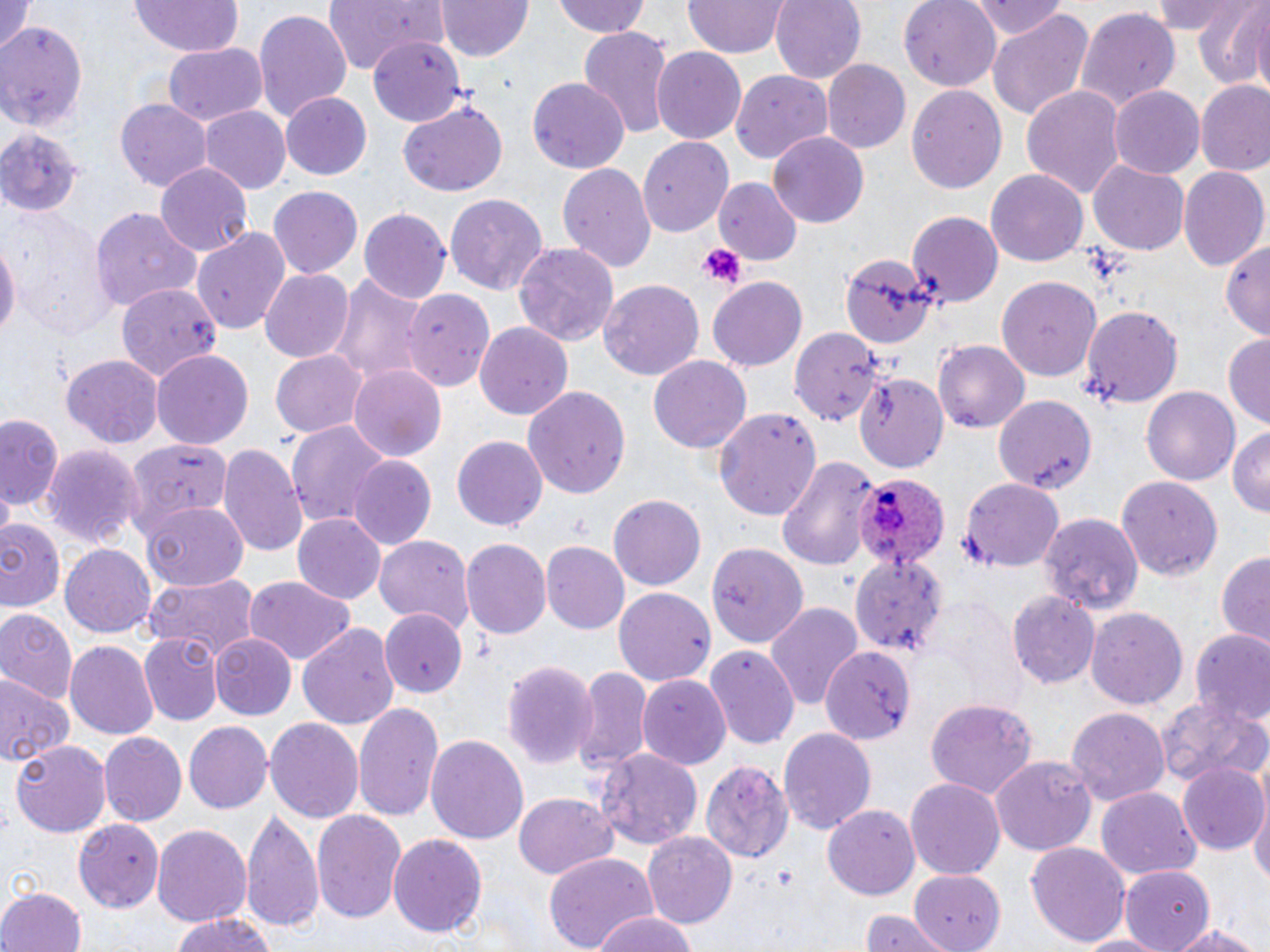
plasmodium_ovale_infected_red_blood_cell_locations: 'approximate bounding boxes as (x1, y1, x2, y2) in pixels: (854, 470, 955, 577)'
slide_level_diagnosis: Plasmodium ovale
modality: light microscopy
field_of_view: one of a larger specimen
platelet_locations: 'approximate bounding boxes as (x1, y1, x2, y2) in pixels: (699, 242, 745, 289)'
uninfected_red_blood_cell_locations: 'approximate bounding boxes as (x1, y1, x2, y2) in pixels: (325, 0, 448, 74), (438, 0, 533, 62), (552, 0, 653, 39), (771, 0, 866, 83), (900, 0, 1003, 89), (975, 0, 1066, 41), (1150, 0, 1252, 36), (1190, 0, 1270, 90), (0, 1, 33, 60), (129, 1, 242, 58), (683, 1, 788, 58), (145, 2, 256, 109), (1244, 6, 1270, 100), (1072, 7, 1182, 114), (253, 8, 353, 122), (987, 8, 1095, 122), (0, 19, 85, 134), (576, 28, 673, 138), (370, 38, 463, 125), (161, 43, 267, 126), (651, 46, 747, 144), (821, 60, 910, 154), (731, 70, 835, 163), (529, 78, 628, 174), (1195, 79, 1270, 175), (907, 83, 1007, 197), (1021, 84, 1127, 200), (1109, 85, 1206, 177), (280, 93, 373, 180), (117, 98, 212, 189), (401, 102, 508, 197), (199, 106, 291, 195), (0, 126, 83, 215), (766, 131, 869, 228), (639, 135, 735, 236), (557, 162, 656, 273), (1088, 162, 1189, 254), (154, 164, 253, 257), (1179, 166, 1269, 270), (988, 169, 1089, 267), (713, 178, 800, 266), (267, 187, 364, 279), (446, 193, 548, 295), (92, 206, 201, 313), (6, 208, 112, 338), (359, 209, 450, 304), (907, 210, 1003, 305), (191, 225, 292, 334), (0, 236, 18, 350), (1220, 238, 1270, 337), (513, 242, 621, 349), (842, 254, 935, 350), (260, 268, 354, 363), (329, 268, 433, 391), (997, 275, 1104, 382), (708, 277, 809, 372), (599, 278, 705, 380), (113, 282, 221, 388), (404, 288, 494, 391), (1083, 305, 1185, 410), (475, 322, 576, 420), (790, 327, 879, 425), (1224, 333, 1270, 430), (934, 340, 1031, 431), (152, 350, 253, 450), (271, 350, 367, 438), (62, 355, 165, 448), (648, 355, 752, 453), (348, 366, 447, 460), (854, 371, 948, 473), (521, 386, 631, 499), (1142, 386, 1242, 486), (993, 394, 1097, 495), (713, 408, 821, 520), (0, 415, 63, 515), (285, 419, 394, 529), (1228, 426, 1270, 520), (453, 436, 547, 531), (123, 438, 238, 534), (219, 442, 310, 560), (40, 443, 144, 550), (776, 455, 879, 569), (348, 456, 436, 550), (1115, 476, 1222, 582), (960, 477, 1065, 571), (610, 495, 706, 590), (142, 502, 249, 593), (1038, 512, 1143, 615), (293, 514, 386, 604), (0, 516, 64, 614), (373, 534, 475, 628), (460, 540, 551, 640), (59, 543, 156, 638), (541, 543, 628, 632), (704, 543, 810, 650), (850, 548, 950, 662), (1215, 553, 1270, 646), (141, 575, 259, 660), (244, 577, 353, 664), (614, 586, 716, 686), (1008, 592, 1101, 689), (932, 596, 1024, 706), (765, 601, 863, 711), (0, 606, 79, 708), (1086, 608, 1188, 711), (379, 609, 466, 695), (296, 623, 402, 731), (1192, 631, 1270, 730), (138, 632, 224, 727), (211, 634, 299, 721), (67, 640, 159, 740), (704, 647, 800, 747), (823, 647, 910, 740), (500, 659, 597, 770), (571, 666, 652, 778), (0, 672, 70, 770), (638, 675, 732, 767), (1156, 695, 1269, 791), (925, 699, 1037, 799), (353, 700, 443, 824), (1068, 708, 1168, 808), (263, 717, 365, 826), (185, 721, 273, 813), (778, 726, 877, 837), (99, 732, 186, 824), (424, 734, 528, 846), (11, 739, 111, 837), (595, 747, 702, 850), (992, 756, 1098, 860), (701, 760, 793, 866), (1178, 763, 1263, 853), (905, 777, 1007, 879), (1098, 789, 1200, 882), (1251, 791, 1270, 888), (513, 793, 619, 881), (821, 804, 919, 900), (311, 807, 407, 927), (241, 809, 324, 931), (73, 819, 163, 914), (151, 823, 254, 929), (641, 830, 737, 927), (390, 834, 487, 939), (1026, 843, 1133, 946), (542, 851, 660, 952), (1118, 867, 1213, 951), (905, 869, 1009, 952), (0, 887, 85, 952), (857, 910, 953, 952), (589, 911, 703, 952), (169, 913, 279, 952), (1165, 918, 1267, 952), (1072, 932, 1175, 951)'
preparation: thin blood smear
image_size: 1270×952 pixels
magnification: 1000x
stain: May-Grünwald-Giemsa